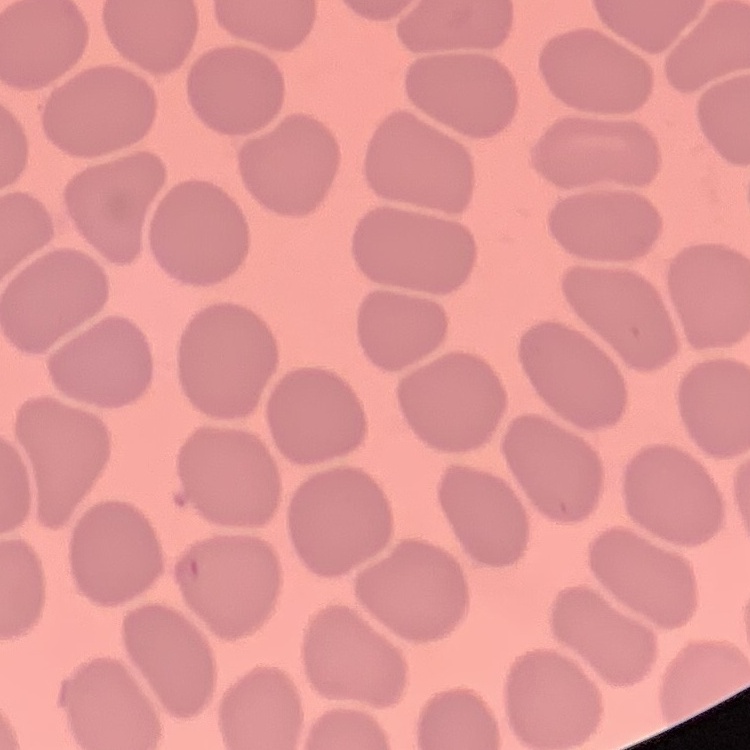

Summary:
  - Red blood cell morphology: no rouleaux formation
  - Image type: one tile cut from a larger photomicrograph
  - Preparation: thin peripheral smear
  - Stain: Field's or Giemsa